Describe the morphology of the erythrocytes.
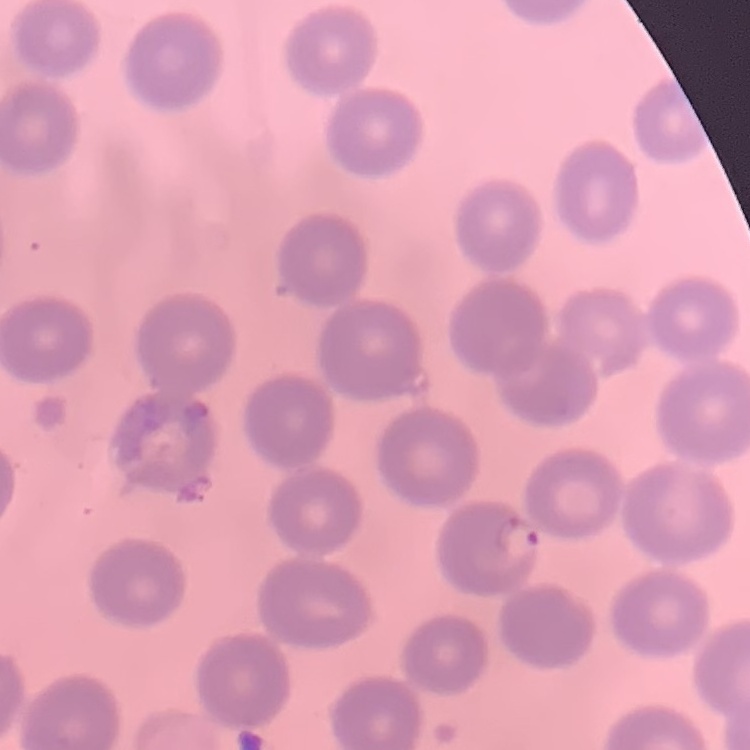
No rouleaux formation.

{
  "stain": "Field's or Giemsa",
  "image_type": "one tile cut from a larger photomicrograph",
  "preparation": "thin peripheral smear"
}